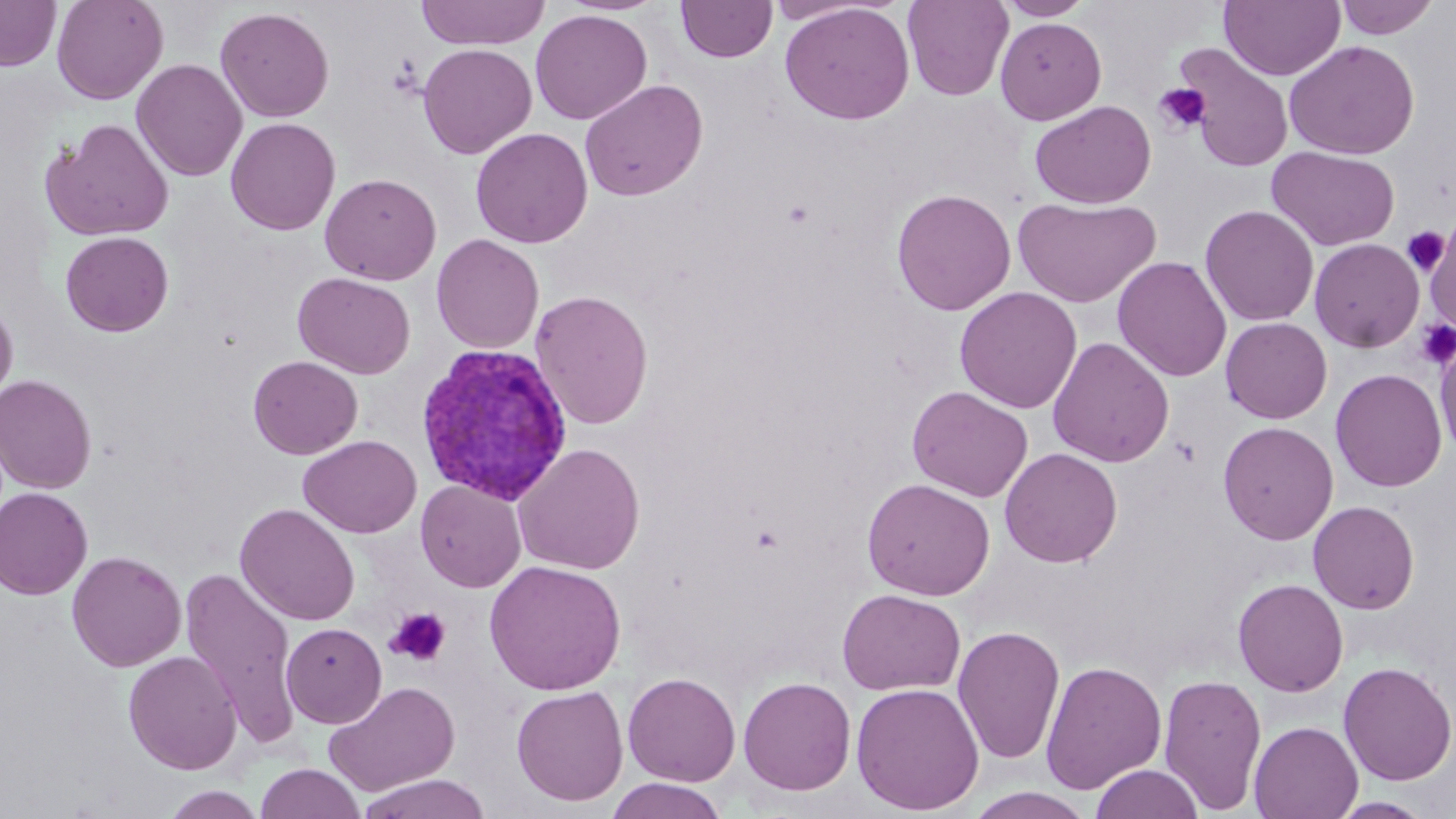
slide_level_diagnosis: Plasmodium vivax
modality: optical microscopy
preparation: thin blood smear
stain: May-Grünwald-Giemsa
magnification: 1000x
image_size: 1456×819 pixels
platelet_locations: 'approximate bounding boxes as (x1, y1, x2, y2) in pixels: (1153, 82, 1212, 135), (1402, 227, 1449, 275), (1414, 319, 1456, 369), (385, 607, 452, 667)'
field_of_view: single
plasmodium_vivax_infected_red_blood_cell_locations: 'approximate bounding boxes as (x1, y1, x2, y2) in pixels: (415, 342, 574, 507)'
uninfected_red_blood_cell_locations: 'approximate bounding boxes as (x1, y1, x2, y2) in pixels: (0, 0, 61, 71), (51, 0, 168, 105), (415, 0, 550, 50), (902, 0, 1013, 101), (996, 0, 1095, 20), (1334, 0, 1440, 40), (676, 1, 777, 63), (1219, 1, 1345, 81), (779, 2, 915, 125), (216, 7, 334, 122), (530, 9, 653, 125), (995, 17, 1107, 124), (1284, 40, 1420, 160), (417, 43, 537, 159), (1174, 43, 1295, 173), (131, 58, 248, 182), (579, 78, 708, 201), (1030, 100, 1157, 209), (225, 117, 341, 235), (42, 118, 175, 241), (470, 127, 593, 248), (1266, 146, 1401, 251), (320, 173, 442, 285), (891, 188, 1016, 316), (1012, 195, 1161, 307), (1200, 205, 1319, 326), (1424, 223, 1456, 331), (60, 231, 174, 337), (431, 234, 544, 354), (1309, 237, 1425, 353), (1112, 255, 1232, 382), (293, 272, 415, 379), (954, 286, 1082, 413), (530, 289, 653, 429), (0, 296, 18, 407), (1220, 317, 1333, 424), (1047, 336, 1174, 468), (1434, 336, 1456, 462), (248, 355, 363, 459), (1330, 368, 1448, 493), (0, 374, 97, 494), (906, 385, 1033, 502), (1217, 421, 1338, 545), (299, 434, 421, 538), (513, 443, 646, 575), (1000, 447, 1123, 568), (861, 478, 995, 600), (416, 480, 526, 592), (0, 487, 93, 599), (1307, 500, 1419, 614), (234, 503, 360, 626), (67, 550, 186, 671), (484, 560, 627, 695), (180, 568, 302, 745), (1232, 578, 1349, 697), (837, 588, 966, 696), (281, 622, 386, 728), (952, 625, 1066, 765), (123, 650, 242, 775), (1040, 660, 1167, 794), (1338, 661, 1456, 785), (623, 672, 741, 787), (1158, 672, 1267, 814), (738, 676, 856, 795), (325, 680, 460, 796), (850, 682, 985, 815), (511, 684, 628, 806), (1249, 720, 1363, 819), (255, 762, 365, 819), (1090, 763, 1205, 819), (356, 773, 491, 819), (605, 778, 727, 818), (162, 786, 266, 819), (965, 787, 1096, 819), (1328, 797, 1436, 818)'